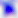

Summary:
  - Magnification: 400x
  - Identification: Toxoplasma gondii
  - Modality: micrograph